Assess this cell for malaria.
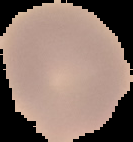

Uninfected.

preparation: thin blood film
image_size: 133×142 pixels
image_type: cell region segmented out of the field of view; surrounding area masked to black